Describe the morphology of the erythrocytes.
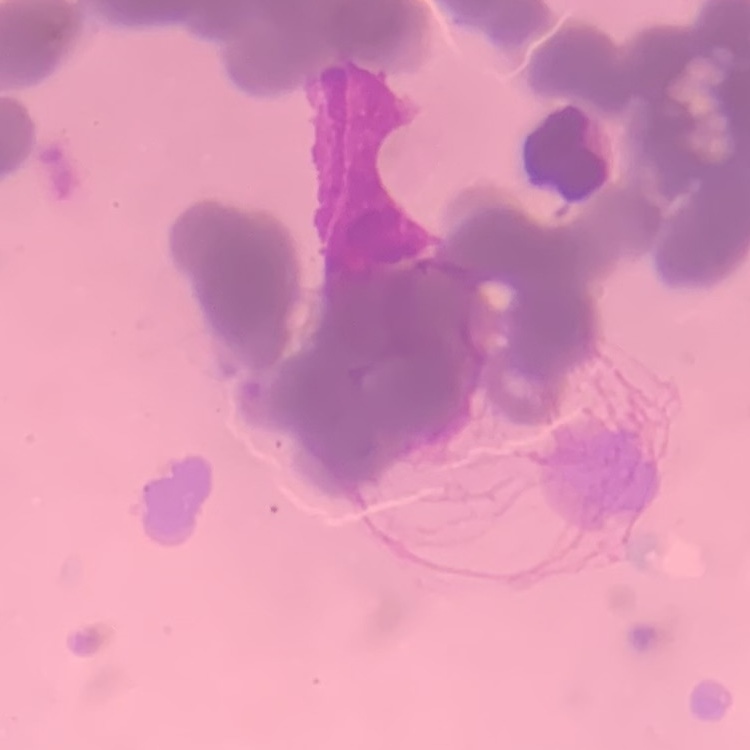
Rouleaux formation.

Thin blood film. Square crop of a larger photomicrograph. Stained with either Field's or Giemsa.